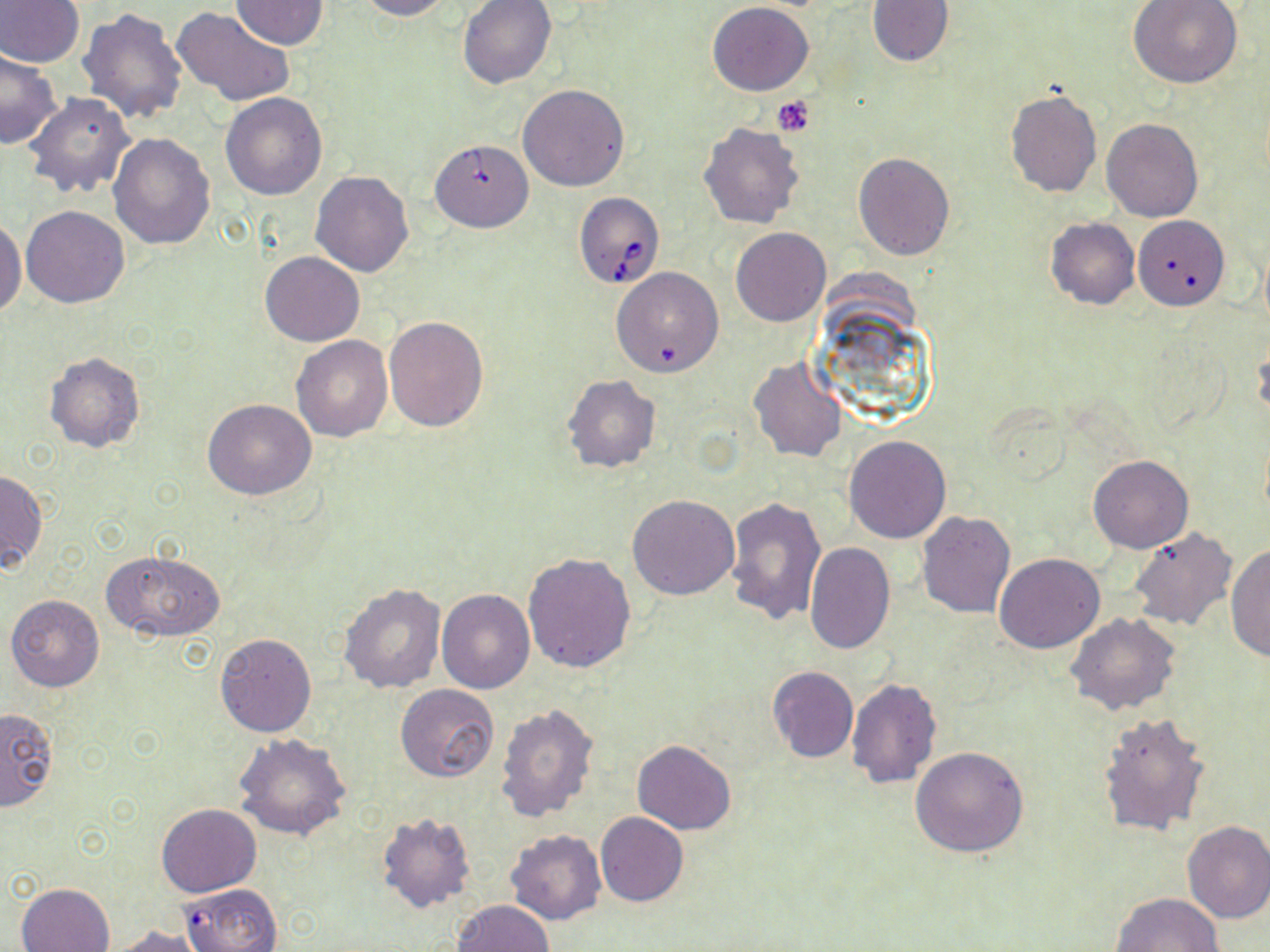

slide_level_diagnosis: Babesia divergens
field_of_view: one of a larger specimen
magnification: 1000x
uninfected_red_blood_cell_locations: 'approximate bounding boxes as named x1/y1/x2/y2 corners in pixels: (x1=0, y1=0, x2=84, y2=67), (x1=231, y1=0, x2=330, y2=50), (x1=355, y1=0, x2=455, y2=21), (x1=457, y1=0, x2=556, y2=88), (x1=1129, y1=0, x2=1242, y2=88), (x1=866, y1=1, x2=952, y2=66), (x1=708, y1=2, x2=812, y2=96), (x1=78, y1=7, x2=188, y2=125), (x1=170, y1=7, x2=295, y2=108), (x1=0, y1=49, x2=63, y2=148), (x1=518, y1=83, x2=629, y2=191), (x1=1005, y1=88, x2=1101, y2=197), (x1=24, y1=91, x2=136, y2=199), (x1=220, y1=93, x2=327, y2=200), (x1=1101, y1=118, x2=1203, y2=222), (x1=699, y1=122, x2=806, y2=230), (x1=108, y1=133, x2=215, y2=250), (x1=853, y1=153, x2=955, y2=260), (x1=309, y1=170, x2=415, y2=277), (x1=21, y1=206, x2=130, y2=309), (x1=0, y1=216, x2=26, y2=318), (x1=1044, y1=218, x2=1140, y2=310), (x1=1137, y1=219, x2=1230, y2=313), (x1=731, y1=228, x2=830, y2=326), (x1=260, y1=251, x2=365, y2=346), (x1=612, y1=267, x2=723, y2=376), (x1=384, y1=316, x2=489, y2=432), (x1=291, y1=335, x2=392, y2=441), (x1=44, y1=353, x2=144, y2=453), (x1=749, y1=358, x2=846, y2=461), (x1=562, y1=375, x2=661, y2=474), (x1=203, y1=399, x2=316, y2=500), (x1=844, y1=436, x2=950, y2=542), (x1=1087, y1=456, x2=1192, y2=553), (x1=1, y1=469, x2=47, y2=574), (x1=628, y1=494, x2=741, y2=599), (x1=723, y1=497, x2=826, y2=626), (x1=915, y1=511, x2=1015, y2=618), (x1=1127, y1=527, x2=1238, y2=632), (x1=1226, y1=542, x2=1270, y2=662), (x1=804, y1=543, x2=894, y2=654), (x1=102, y1=551, x2=226, y2=643), (x1=523, y1=551, x2=637, y2=673), (x1=993, y1=553, x2=1104, y2=652), (x1=338, y1=583, x2=447, y2=694), (x1=437, y1=589, x2=534, y2=693), (x1=6, y1=593, x2=105, y2=692), (x1=1066, y1=611, x2=1180, y2=716), (x1=213, y1=633, x2=317, y2=738), (x1=766, y1=666, x2=858, y2=764), (x1=845, y1=678, x2=942, y2=788), (x1=396, y1=685, x2=498, y2=782), (x1=495, y1=702, x2=601, y2=824), (x1=0, y1=706, x2=57, y2=811), (x1=1096, y1=711, x2=1211, y2=838), (x1=234, y1=734, x2=351, y2=842), (x1=632, y1=740, x2=738, y2=835), (x1=912, y1=745, x2=1029, y2=857), (x1=156, y1=804, x2=262, y2=898), (x1=375, y1=811, x2=477, y2=915), (x1=596, y1=813, x2=688, y2=908), (x1=1182, y1=819, x2=1270, y2=924), (x1=505, y1=829, x2=608, y2=925), (x1=17, y1=882, x2=115, y2=951), (x1=1111, y1=892, x2=1224, y2=952), (x1=454, y1=900, x2=553, y2=952), (x1=106, y1=926, x2=208, y2=951)'
image_size: 1270×952 pixels
stain: May-Grünwald-Giemsa
modality: light microscopy
babesia_divergens_infected_red_blood_cell_locations: 'approximate bounding boxes as named x1/y1/x2/y2 corners in pixels: (x1=431, y1=141, x2=537, y2=234), (x1=573, y1=193, x2=664, y2=289), (x1=171, y1=882, x2=281, y2=952)'
platelet_locations: 'approximate bounding boxes as named x1/y1/x2/y2 corners in pixels: (x1=772, y1=96, x2=815, y2=135)'
preparation: thin blood smear